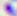

Summary:
  - Modality: photomicrograph
  - Identification: Toxoplasma gondii
  - Magnification: 400x